Assess for malaria.
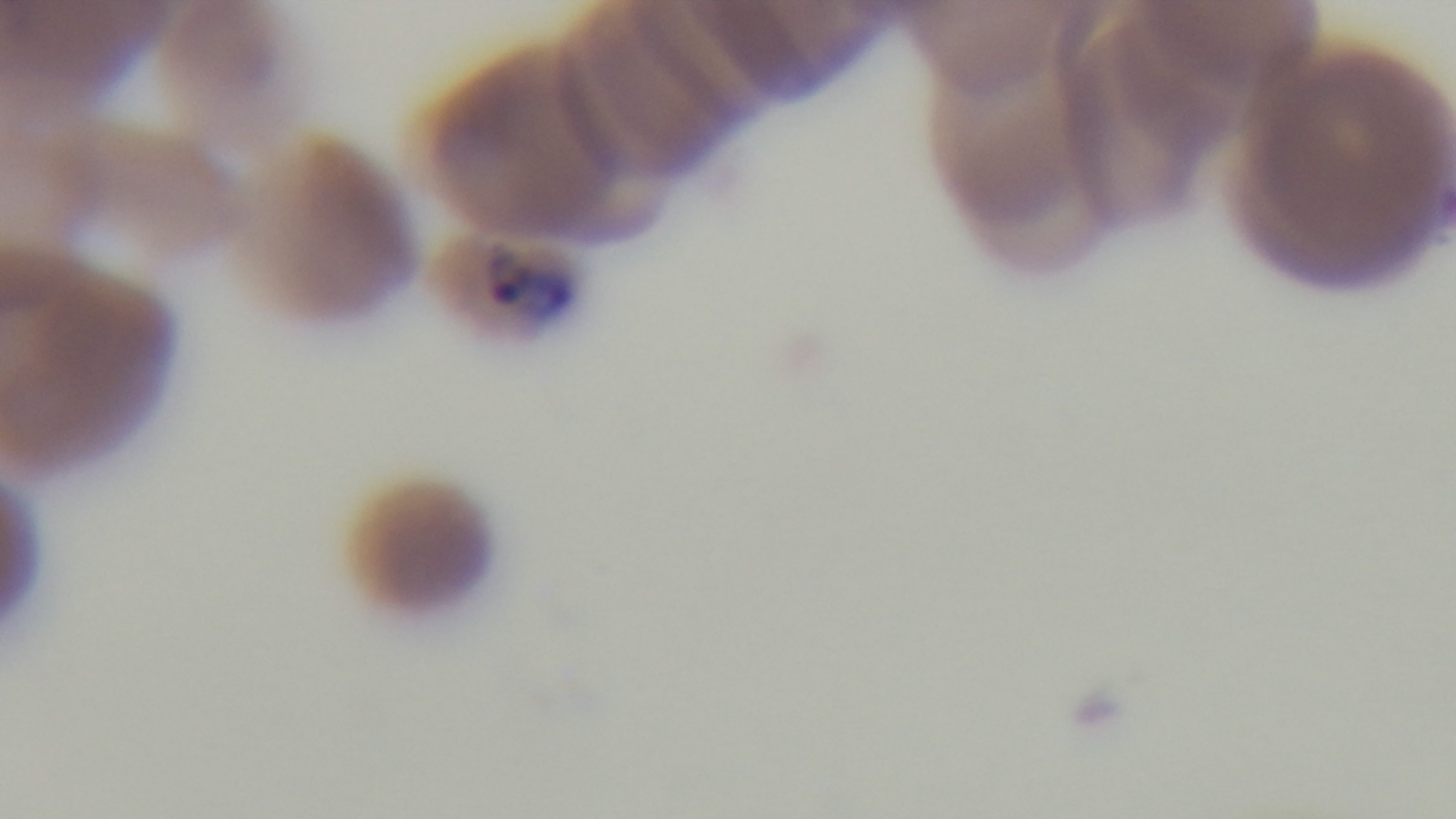

It is infected.

{
  "preparation": "thin blood film",
  "stain": "Giemsa",
  "field_of_view": "single",
  "capture": "mounted 4K digital camera",
  "objective": "100x oil immersion",
  "modality": "light microscopy"
}